Report the malaria status of this cell.
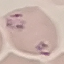
It is parasitized.

Giemsa-stained preparation. Automatically extracted cell patch, resized to 64 × 64 pixels. Thin smear of blood. Acquired by smartphone through the microscope eyepiece.